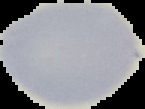 From a thin blood film. Malaria status: uninfected. The area outside the segmented cell region is set to black. Image is 145×109 pixels.